Classify this cell by malaria status.
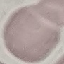
Uninfected.

{
  "preparation": "thin blood smear",
  "stain": "Giemsa",
  "image_type": "cell patch, automatically extracted from a larger field of view and resized to 64 × 64 pixels",
  "capture": "smartphone through the microscope eyepiece"
}